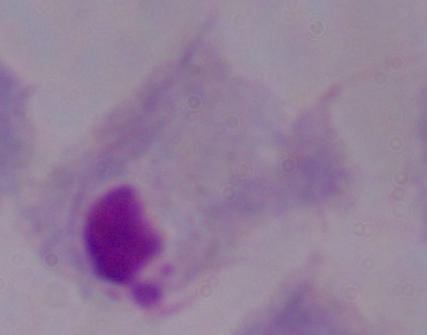

magnification = 1000x
modality = photomicrograph
identification = trichomonad